Give the position of every malaria parasite and every leukocyte.
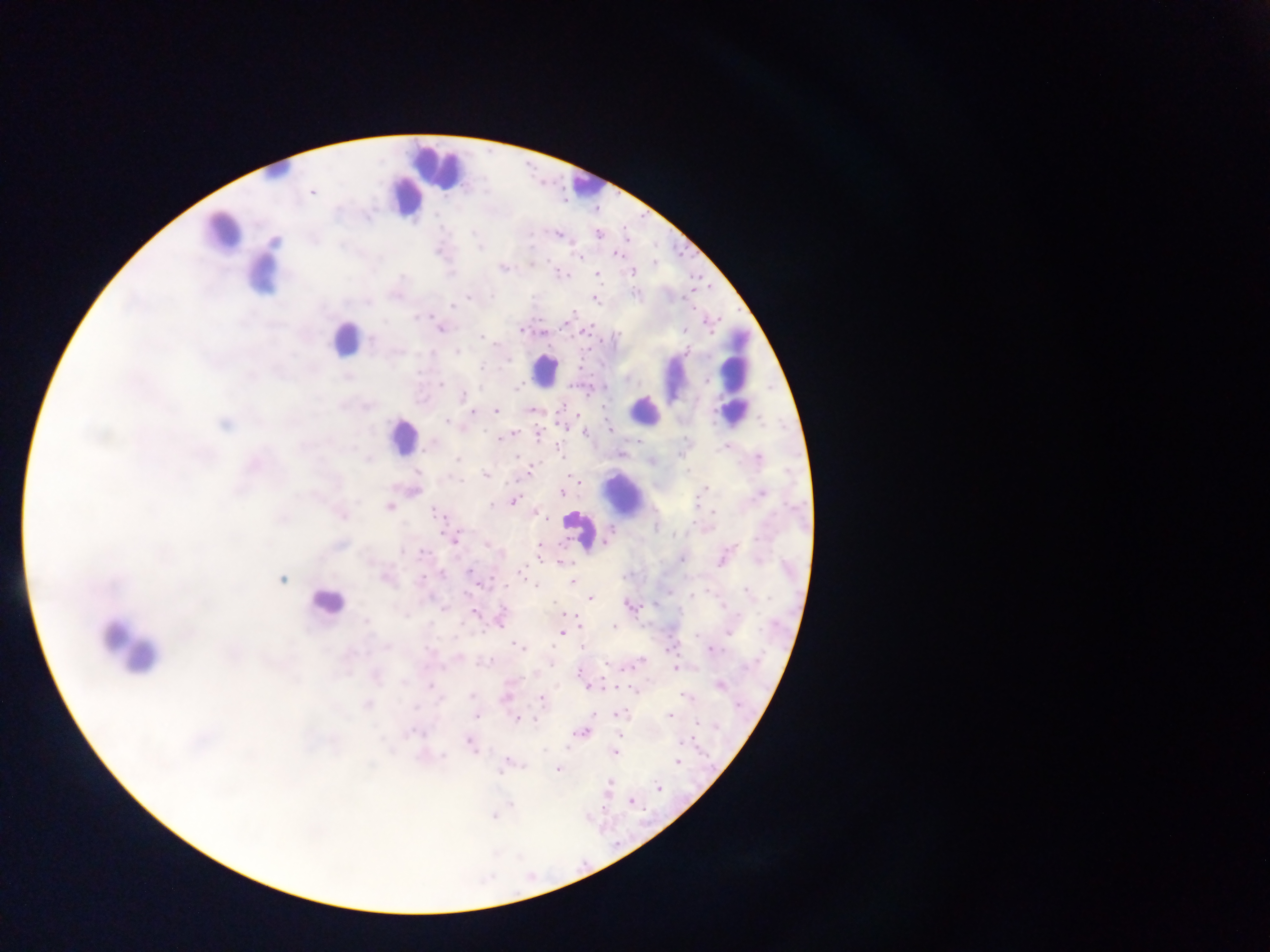
Approximate centers as [x, y] in pixels.
Malaria parasites: [312, 192], [472, 233], [597, 234], [558, 235], [275, 242], [480, 247], [615, 254], [580, 256], [531, 264], [502, 268], [632, 271], [561, 274], [597, 274], [402, 277], [634, 293], [491, 296], [469, 297], [595, 300], [368, 302], [452, 305], [572, 312], [416, 318], [566, 323], [440, 329], [520, 331], [685, 331], [542, 332], [482, 336], [372, 339], [686, 351], [457, 352], [508, 359], [482, 367], [441, 384], [517, 388], [464, 395], [531, 410], [496, 411], [471, 412], [446, 421], [224, 425], [563, 428], [609, 429], [586, 431], [511, 434], [538, 435], [507, 437], [499, 438], [639, 441], [426, 447], [725, 447], [560, 452], [518, 455], [759, 458], [457, 459], [369, 460], [531, 469], [417, 472], [485, 475], [459, 479], [704, 490], [562, 492], [761, 494], [358, 501], [514, 501], [492, 506], [388, 507], [435, 513], [712, 513], [342, 515], [545, 517], [284, 519], [454, 538], [759, 538], [607, 541], [423, 552], [539, 552], [402, 553], [681, 559], [721, 561], [562, 563], [442, 572], [470, 572], [520, 572], [422, 577], [386, 578], [282, 580], [572, 582], [536, 584], [747, 591], [691, 596], [590, 598], [629, 605], [475, 613], [366, 621], [614, 626], [561, 632], [729, 632], [189, 633], [696, 636], [514, 644], [518, 646], [582, 646], [387, 647], [426, 649], [712, 649], [490, 660], [606, 665], [676, 668], [579, 672], [375, 677], [404, 682], [720, 684], [431, 686], [635, 691], [472, 696], [682, 696], [505, 698], [541, 700], [368, 705], [415, 707], [593, 714], [617, 714], [669, 715], [477, 716], [517, 719], [535, 720], [697, 722], [581, 732], [412, 733], [620, 734], [681, 742], [470, 743], [615, 752], [443, 755], [677, 762], [505, 764], [558, 770], [608, 784], [658, 787], [631, 801], [512, 804], [493, 816].
Leukocytes: [436, 164], [275, 175], [586, 184], [404, 194], [221, 231], [261, 276], [344, 340], [547, 368], [735, 369], [675, 378], [645, 410], [401, 436], [624, 494], [579, 535], [324, 603], [126, 646].

Photographed through a microscope with a mobile-phone camera. Image is 1270×952 pixels. Sample from Ghana. Thick blood smear. Single field of view.